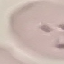
Malaria status: parasitized. Cell patch, automatically extracted from a larger field of view and resized to 64 × 64 pixels. Giemsa stain. Acquired by smartphone through the microscope eyepiece. Thin blood film.